Describe the morphology of the red blood cells.
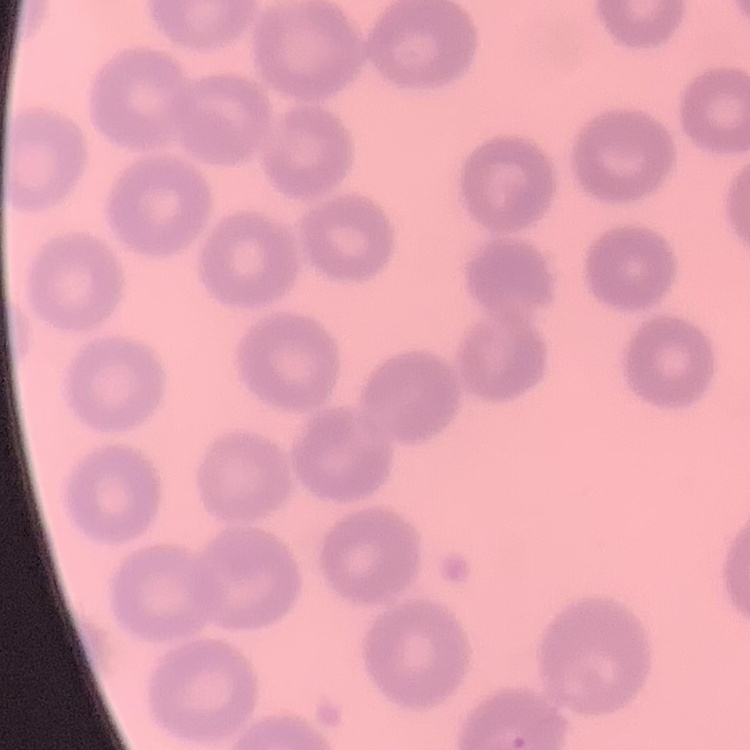
They show no rouleaux formation.

Summary:
  - Image type: one tile cut from a larger photomicrograph
  - Preparation: thin peripheral smear
  - Stain: Field's or Giemsa